Name the parasite shown.
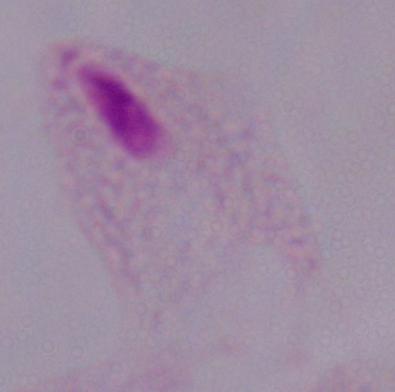
A trichomonad.

magnification: 1000x
modality: photomicrograph